Classify this cell by malaria status.
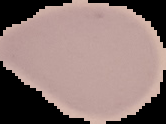
It is uninfected.

image size = 166×124 pixels
image type = segmented cell region on a black background
preparation = thin blood smear